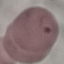

{
  "result": "malaria parasites identified",
  "image_type": "cell patch, automatically extracted from a larger field of view and resized to 64 × 64 pixels",
  "stain": "Giemsa",
  "preparation": "thin smear",
  "capture": "smartphone camera at the microscope eyepiece"
}